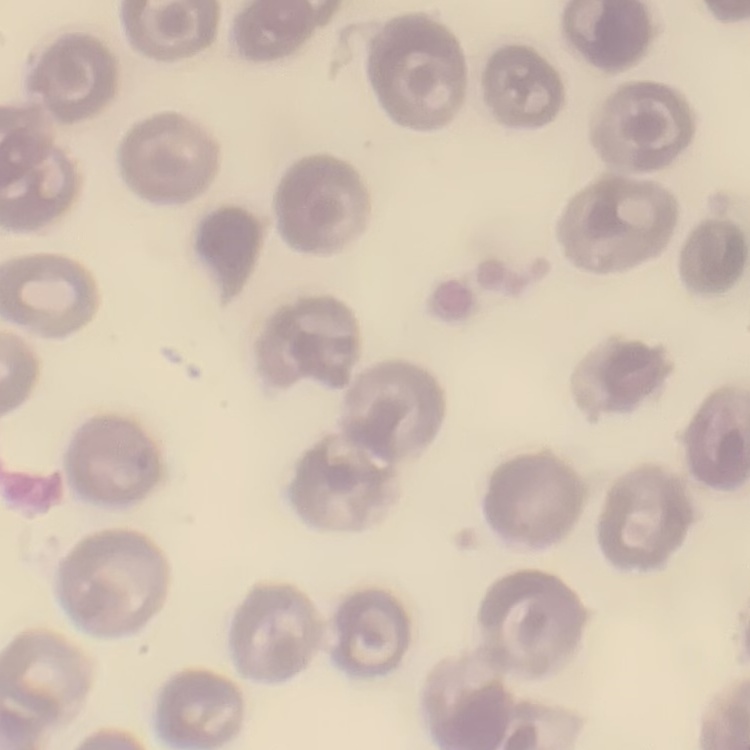
Summary:
  - Erythrocyte morphology: no rouleaux formation
  - Stain: Field's or Giemsa
  - Preparation: thin peripheral smear
  - Image type: one tile cut from a larger photomicrograph